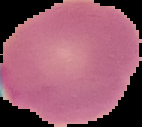

image_size: 142×127 pixels
image_type: cell region segmented out of the field of view; surrounding area masked to black
malaria_status: uninfected
preparation: thin blood smear